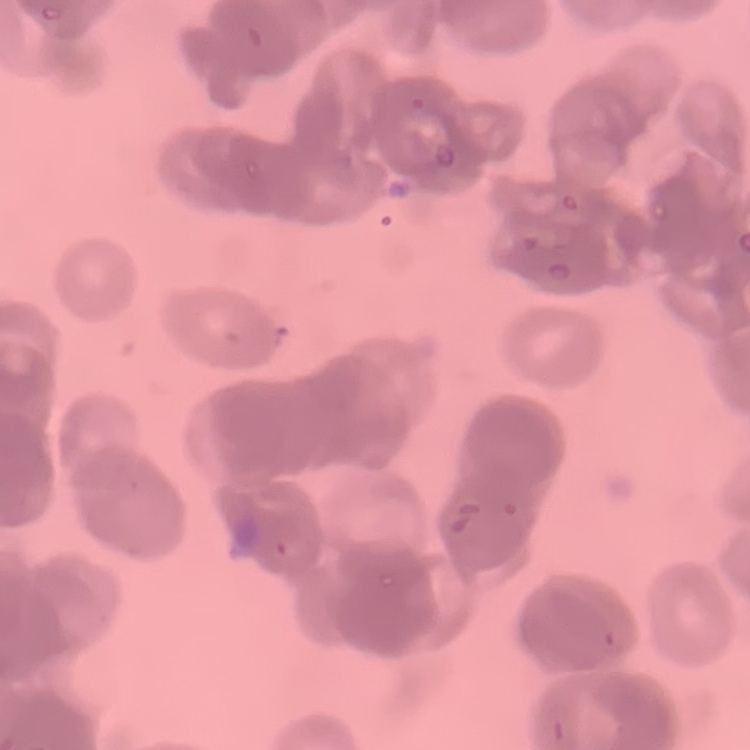
The erythrocytes exhibit rouleaux formation. Square crop of a larger photomicrograph. Field's or Giemsa stain. Thin blood smear.